Assess the morphology of the erythrocytes.
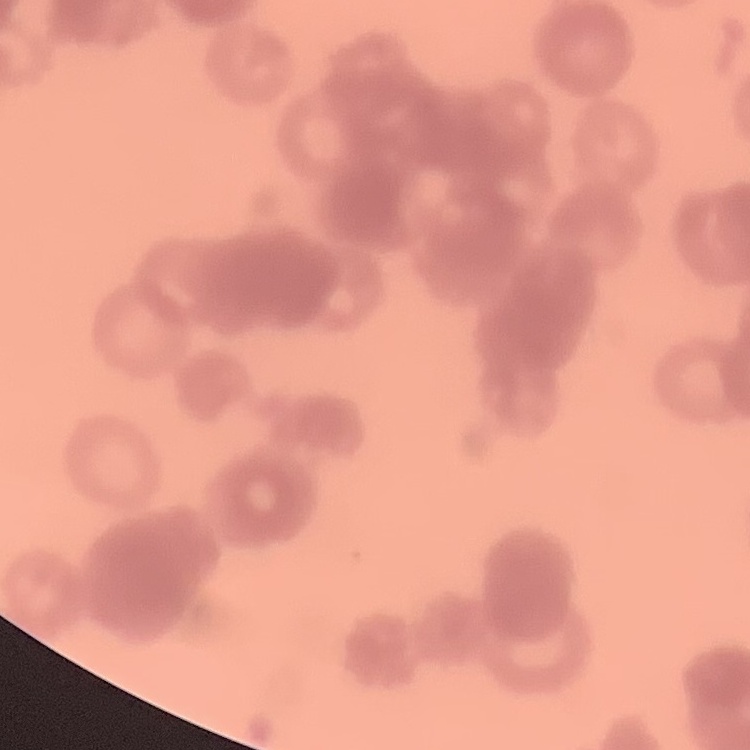

They show rouleaux formation.

{
  "preparation": "thin blood smear",
  "stain": "Field's or Giemsa",
  "image_type": "square crop of a larger photomicrograph"
}